Identify the blood parasite species.
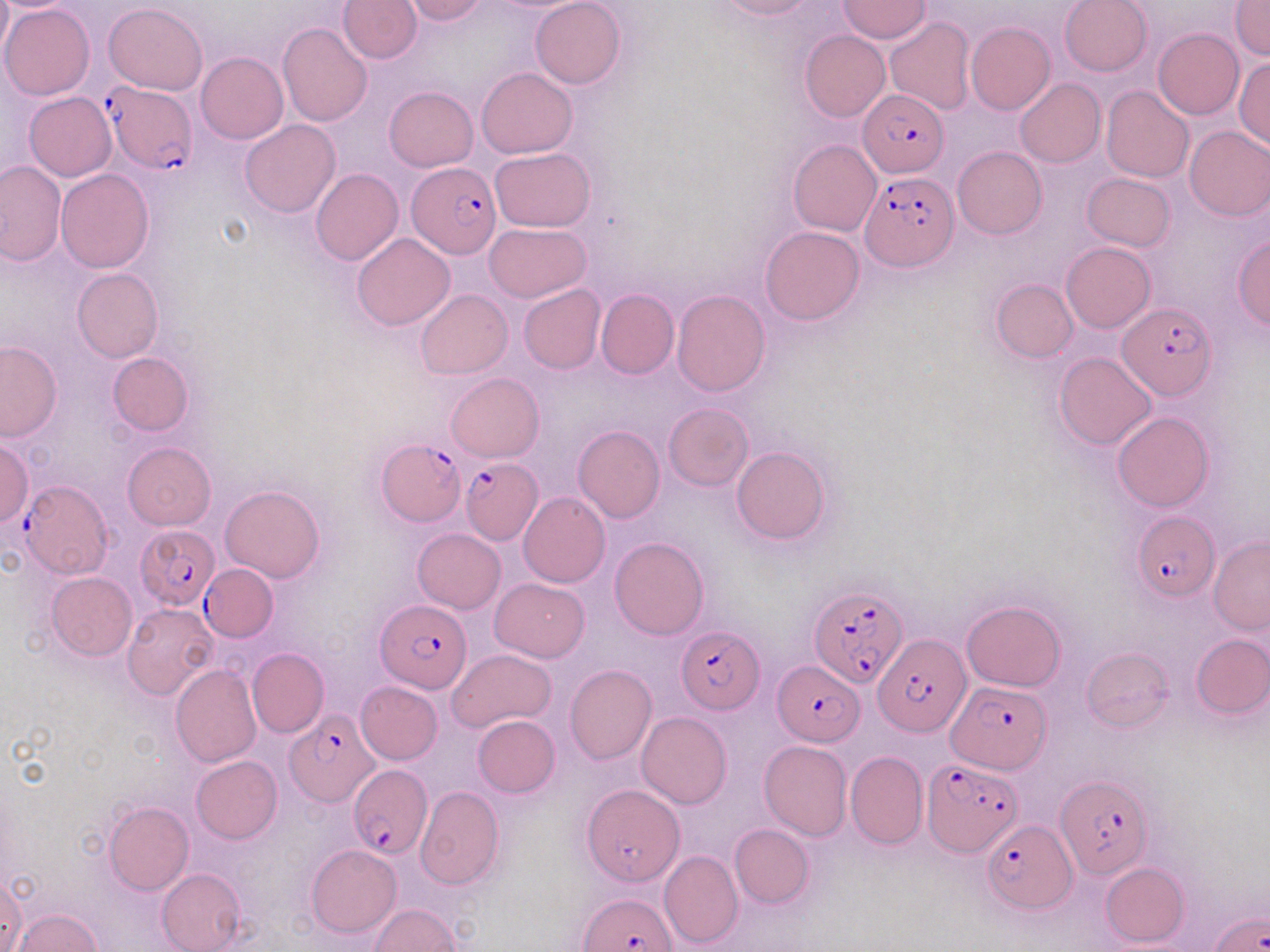

Plasmodium falciparum.

Summary:
  - Coordinate format: approximate bounding boxes as [x1, y1, x2, y2] in pixels
  - Plasmodium falciparum-infected red blood cell locations: [101, 80, 195, 174], [858, 90, 950, 178], [407, 164, 500, 259], [859, 171, 957, 272], [1118, 301, 1217, 399], [377, 439, 464, 525], [456, 458, 541, 543], [20, 480, 113, 579], [1130, 510, 1220, 602], [136, 524, 220, 608], [200, 564, 278, 641], [811, 582, 909, 687], [375, 599, 473, 692], [677, 626, 764, 713], [873, 632, 971, 738], [771, 662, 861, 746], [949, 681, 1052, 774], [284, 710, 378, 807], [922, 758, 1023, 856], [349, 765, 430, 857], [1057, 774, 1152, 879], [983, 818, 1075, 911], [580, 894, 677, 952], [1209, 908, 1268, 952]
  - Uninfected red blood cell locations: [337, 0, 423, 63], [404, 0, 488, 24], [530, 0, 625, 88], [714, 0, 819, 20], [1058, 0, 1152, 76], [838, 1, 931, 42], [1231, 2, 1270, 59], [1, 3, 95, 100], [103, 3, 209, 94], [883, 16, 977, 117], [277, 21, 372, 127], [966, 22, 1055, 114], [1152, 29, 1243, 120], [800, 30, 890, 122], [196, 51, 288, 145], [1234, 57, 1270, 150], [477, 68, 577, 158], [1014, 77, 1105, 168], [1101, 85, 1194, 182], [384, 86, 477, 170], [24, 92, 116, 181], [240, 120, 340, 218], [1184, 126, 1270, 221], [788, 139, 882, 236], [953, 146, 1046, 239], [489, 147, 597, 231], [0, 161, 65, 265], [55, 168, 154, 272], [311, 168, 403, 265], [1081, 173, 1175, 251], [483, 223, 592, 302], [760, 226, 865, 325], [352, 232, 455, 330], [1231, 235, 1270, 327], [1061, 242, 1155, 333], [71, 267, 162, 362], [991, 279, 1077, 361], [518, 283, 605, 374], [416, 289, 512, 378], [596, 289, 678, 378], [672, 289, 770, 396], [1, 341, 63, 442], [107, 352, 193, 436], [1056, 353, 1156, 449], [446, 373, 544, 461], [664, 403, 753, 490], [1112, 411, 1213, 512], [572, 425, 665, 523], [0, 439, 33, 528], [124, 442, 216, 529], [731, 446, 831, 545], [219, 486, 326, 582], [518, 492, 611, 588], [413, 528, 505, 613], [1208, 535, 1270, 634], [610, 536, 709, 640], [46, 572, 137, 661], [491, 578, 588, 661], [961, 600, 1065, 692], [122, 603, 217, 701], [1191, 635, 1270, 718], [1081, 647, 1175, 732], [248, 648, 329, 738], [445, 648, 556, 734], [171, 664, 261, 768], [565, 664, 656, 765], [356, 681, 443, 764], [636, 712, 732, 809], [472, 715, 560, 797], [759, 740, 852, 840], [845, 750, 927, 849], [191, 755, 282, 843], [581, 785, 684, 887], [416, 786, 504, 889], [103, 801, 193, 894], [730, 824, 813, 907], [306, 844, 401, 938], [665, 847, 747, 946], [1101, 861, 1189, 946], [156, 868, 247, 951], [0, 873, 28, 952], [369, 903, 461, 951], [14, 909, 103, 951]
  - Field of view: one of a larger specimen
  - Image size: 1270×952 pixels
  - Preparation: thin blood smear
  - Modality: light microscopy
  - Stain: May-Grünwald-Giemsa
  - Magnification: 1000x